Give the position of each Plasmodium falciparum parasite with its life-cycle stage, each leukocyte, and any debris.
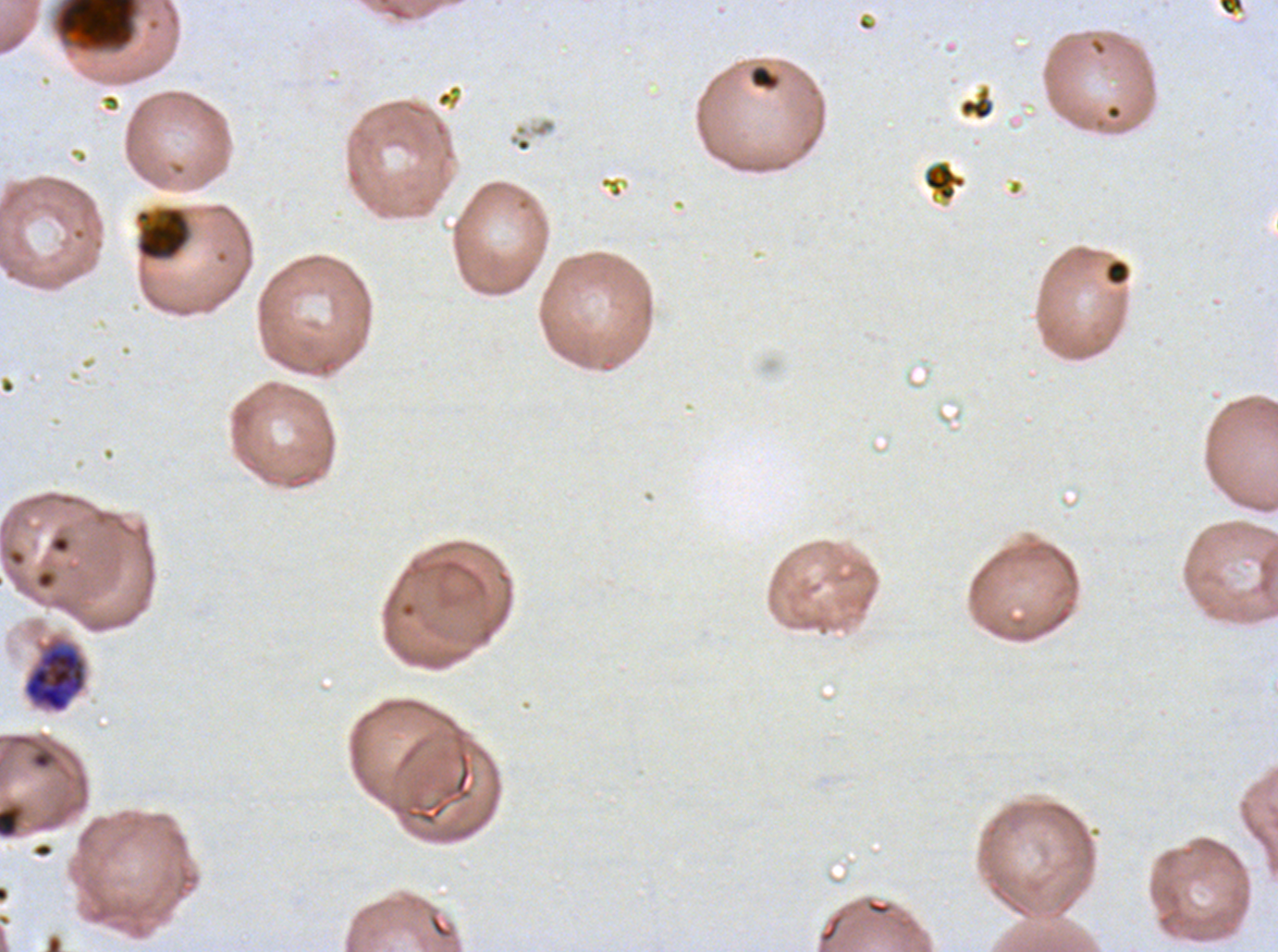
Approximate bounding rectangles given as corner coordinates in pixels from the top-left.
Late trophozoites: (x1=22, y1=638, x2=87, y2=714).
Debris: (x1=55, y1=0, x2=139, y2=52), (x1=748, y1=64, x2=780, y2=91), (x1=959, y1=87, x2=995, y2=121), (x1=923, y1=161, x2=967, y2=202), (x1=135, y1=205, x2=191, y2=262), (x1=1106, y1=260, x2=1128, y2=285).
No rings, late-ring/early-trophozoite forms, mid trophozoites, early schizonts, late schizonts, segmenters, gametocytes, or leukocytes observed.

Summary:
  - Specimen: Plasmodium falciparum cultured ex vivo for 24 to 48 hours, from a patient in The Gambia
  - Field of view: one sub-image of a larger composite
  - Stain: Giemsa
  - Image size: 1278×952 pixels
  - Preparation: thin blood film